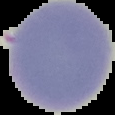

Result: negative for malaria parasites. Cell region segmented out of the field of view; the surrounding area is masked to black. Image is 115×115 pixels. From a thin blood smear.